Classify this cell by malaria status.
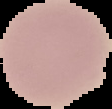

Uninfected.

preparation = thin blood smear
image type = cell region segmented out of the field of view; surrounding area masked to black
image size = 112×109 pixels